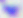

Toxoplasma gondii is shown. Photomicrograph. Captured at 400x magnification.